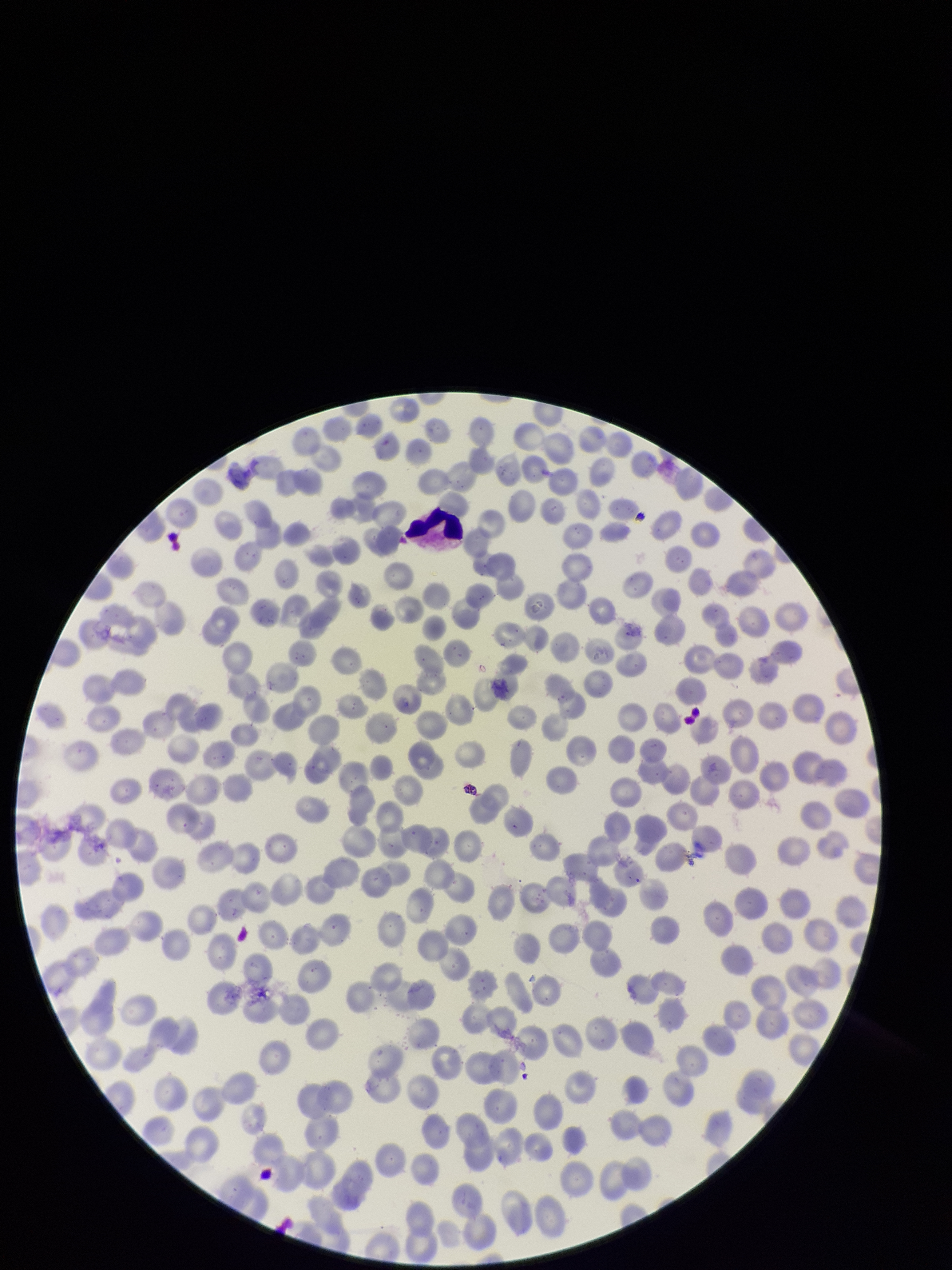

parasitized_red_blood_cells: none detected
parasitized_red_blood_cell_count: 0
image_size: 952×1270 pixels
species_reported_for_this_patient: Plasmodium falciparum
red_blood_cell_count: 320
capture: smartphone photograph through the microscope eyepiece
preparation: thin smear
stain: Giemsa
field_of_view: one from this slide
patient_malaria_status: infected